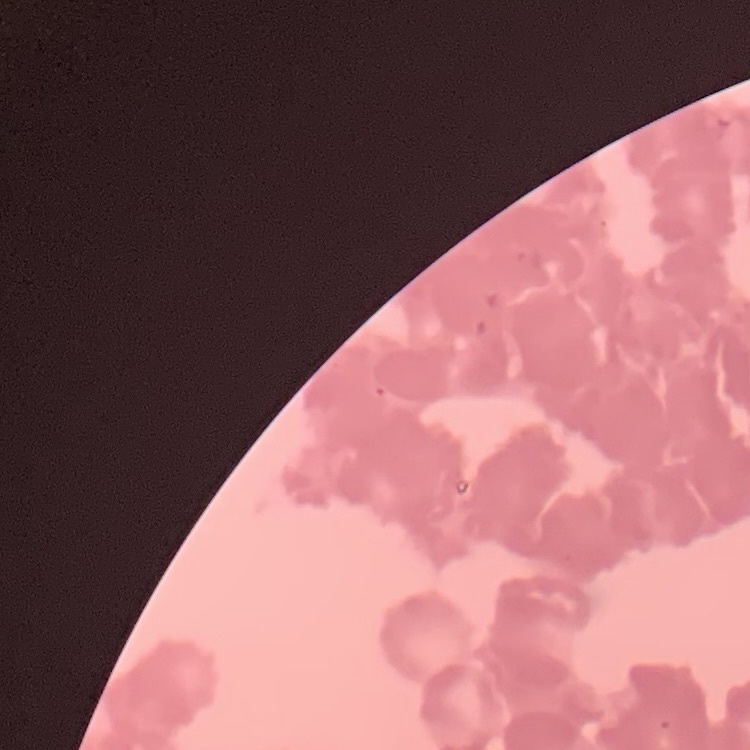

Summary:
  - Erythrocyte morphology: rouleaux formation
  - Image type: square crop of a larger photomicrograph
  - Stain: Field's or Giemsa
  - Preparation: thin blood smear